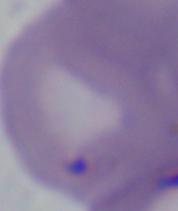
modality: photomicrograph
magnification: 1000x
identification: Babesia